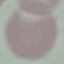 Malaria status: uninfected. Acquired by smartphone through the microscope eyepiece. Giemsa stain. Cell patch, automatically extracted from a larger field of view and resized to 64 × 64 pixels. Thin blood film.